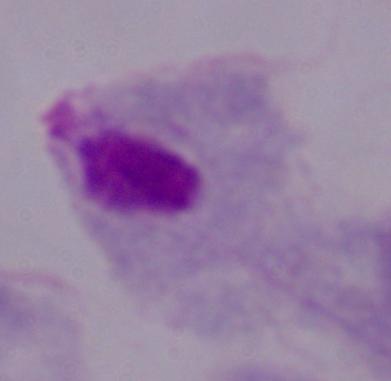

magnification = 1000x
identification = trichomonad
modality = photomicrograph